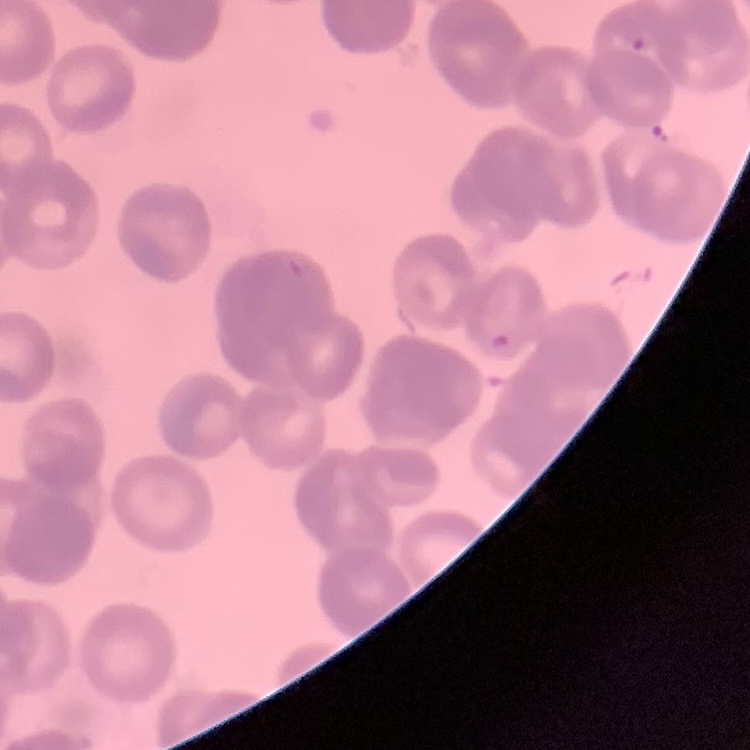
Summary:
  - Red blood cell morphology: rouleaux formation
  - Image type: square crop of a larger photomicrograph
  - Stain: Field's or Giemsa
  - Preparation: thin peripheral smear